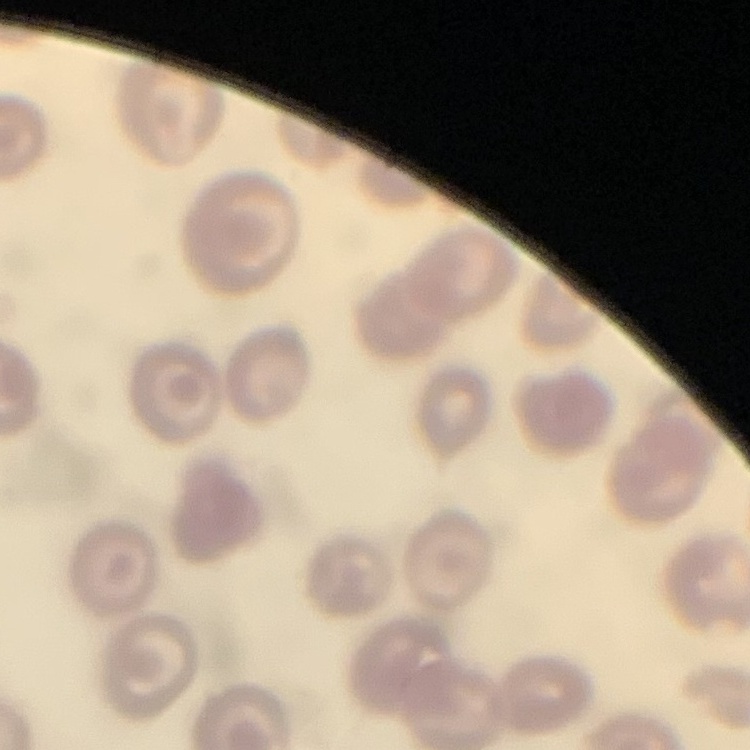
Summary:
  - Erythrocyte morphology: no rouleaux formation
  - Image type: square crop of a larger photomicrograph
  - Stain: Field's or Giemsa
  - Preparation: thin blood film